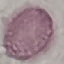 Result: negative for malaria parasites. Photographed with a smartphone camera at the microscope eyepiece. Thin blood smear. Cell patch, automatically extracted from a larger field of view and resized to 64 × 64 pixels. Giemsa stain.